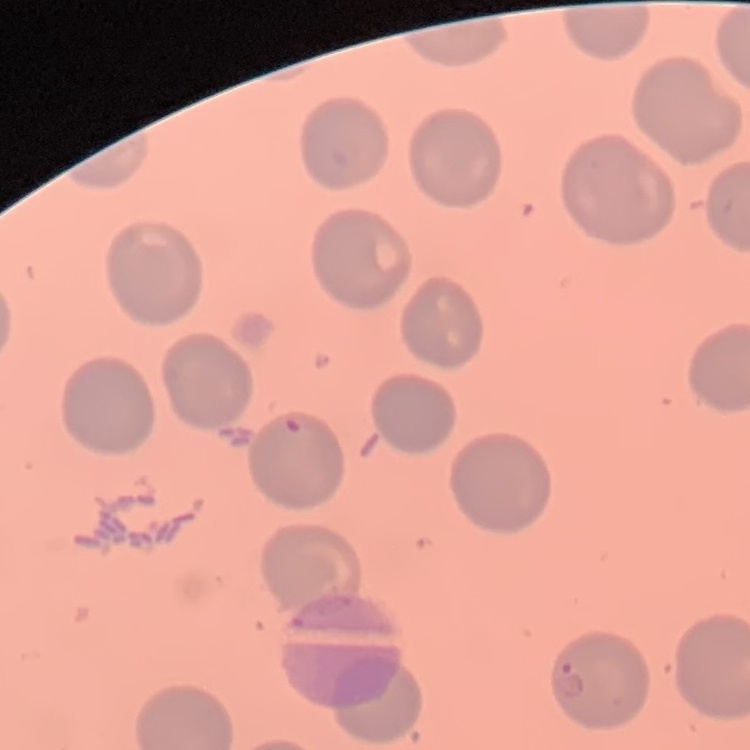

Summary:
  - Erythrocyte morphology: no rouleaux formation
  - Preparation: thin blood film
  - Stain: Field's or Giemsa
  - Image type: square crop of a larger photomicrograph